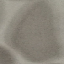

result = negative for malaria parasites
capture = smartphone through the microscope eyepiece
preparation = thin smear
stain = Giemsa
image type = automatically extracted cell patch, resized to 64 × 64 pixels